Describe the morphology of the erythrocytes.
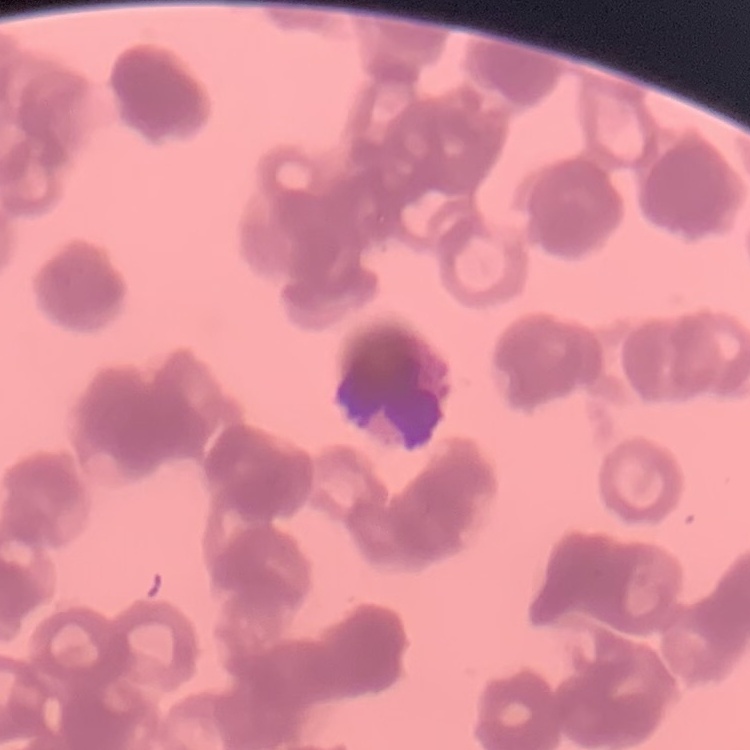
Rouleaux formation.

One tile cut from a larger photomicrograph. Stained with either Field's or Giemsa. Thin peripheral smear.